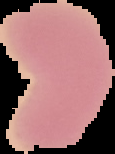

preparation = thin blood film
image type = segmented cell region with the area outside set to black
image size = 115×154 pixels
result = no malaria parasites seen